Assess this cell for malaria.
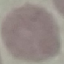

It is uninfected.

capture = smartphone through the microscope eyepiece
preparation = thin blood smear
image type = automatically extracted cell patch, resized to 64 × 64 pixels
stain = Giemsa